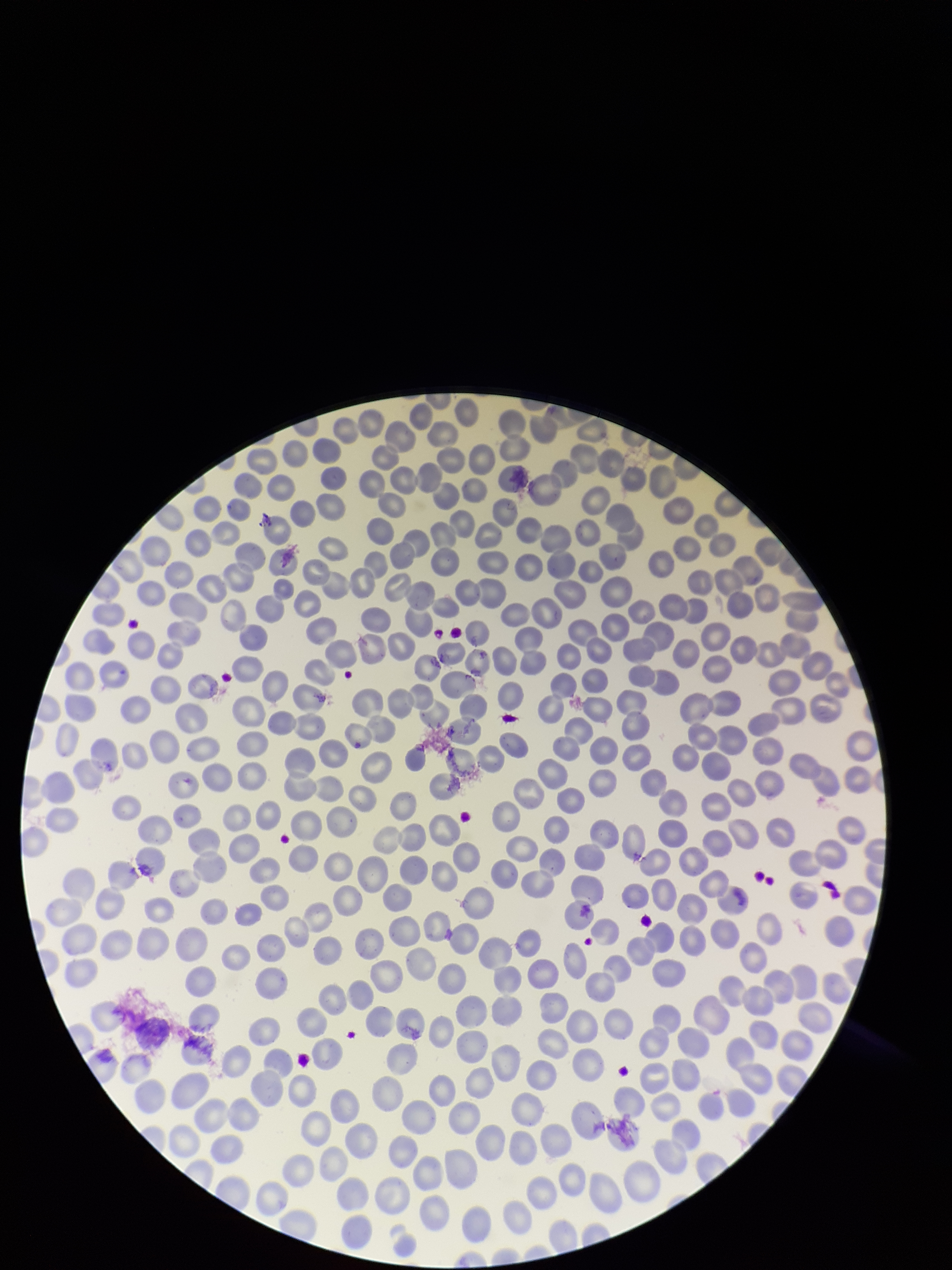

parasitized red blood cells = none seen
preparation = thin smear
parasitized red blood cell count = 0
field of view = single
stain = Giemsa
species reported for this patient = Plasmodium falciparum
patient malaria status = positive
capture = smartphone photograph through the microscope eyepiece
image size = 952×1270 pixels
red blood cell count = 343